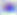

Toxoplasma gondii is shown. 400x magnification. Photomicrograph.